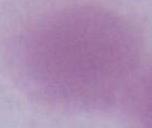

identification = erythrocyte
modality = micrograph
magnification = 1000x